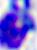
Photomicrograph. A white blood cell is shown. Captured at 400x magnification.